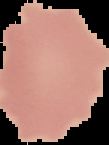

Summary:
  - Preparation: thin blood smear
  - Result: no Plasmodium parasites seen
  - Image size: 109×145 pixels
  - Image type: segmented cell region with the area outside set to black